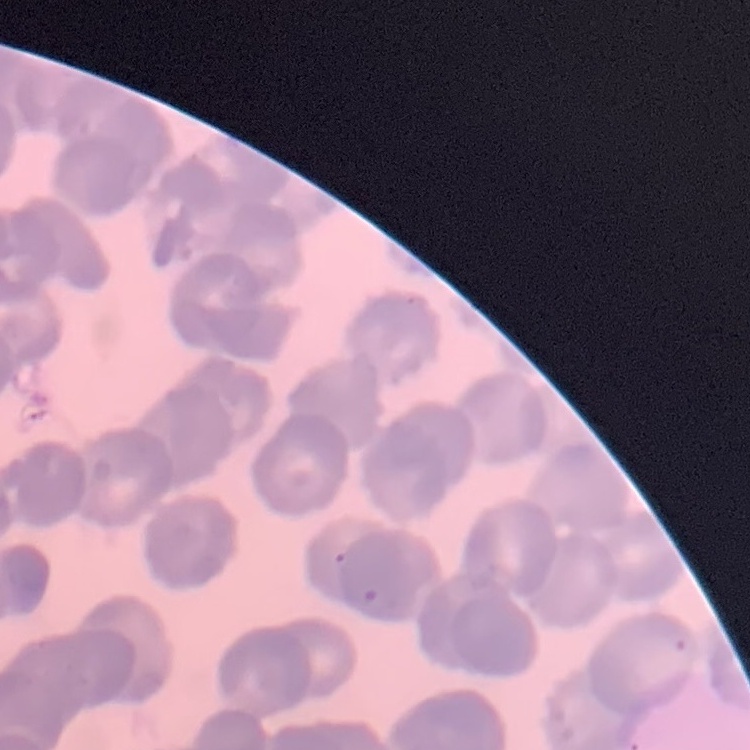

Summary:
  - Red blood cell morphology: rouleaux formation
  - Preparation: thin blood smear
  - Image type: one tile cut from a larger photomicrograph
  - Stain: Field's or Giemsa